Give the position of every leukocyte visible.
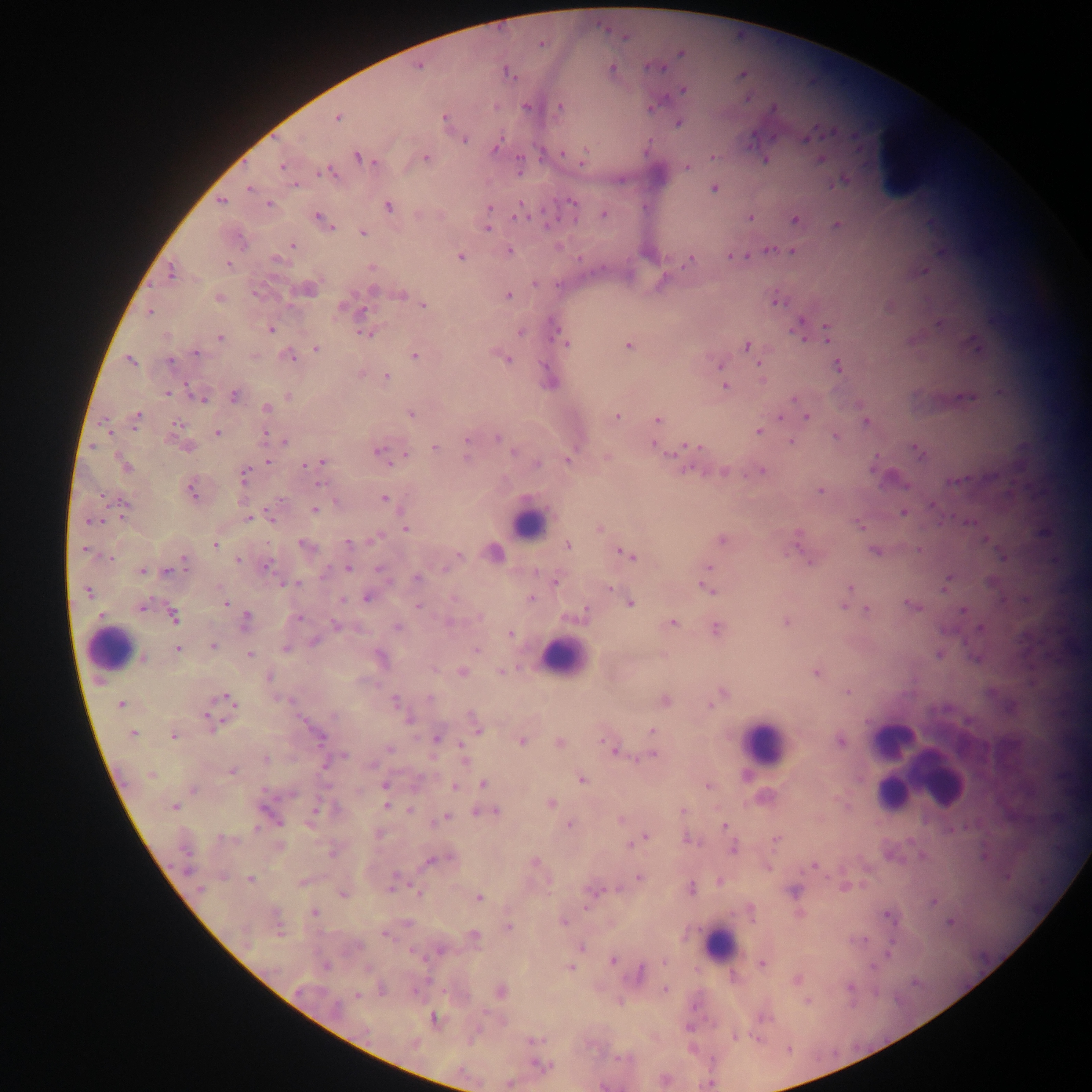

Approximate centers as (x, y) in pixels.
Leukocytes: (534, 523), (121, 652), (560, 660), (888, 740), (768, 750), (937, 779), (894, 795), (718, 946).

Summary:
  - Malaria parasite locations: (623, 37), (540, 44), (649, 66), (613, 67), (661, 67), (507, 72), (742, 74), (513, 79), (683, 90), (746, 99), (526, 105), (561, 105), (495, 106), (655, 106), (771, 110), (444, 117), (337, 118), (678, 123), (836, 132), (807, 139), (466, 140), (751, 144), (496, 146), (586, 150), (563, 153), (358, 156), (519, 158), (713, 158), (821, 158), (427, 159), (766, 160), (374, 161), (583, 162), (282, 166), (687, 166), (330, 167), (323, 172), (317, 174), (842, 179), (296, 184), (834, 184), (714, 187), (248, 189), (222, 200), (571, 201), (521, 202), (268, 203), (388, 205), (489, 207), (546, 207), (604, 213), (317, 215), (514, 216), (750, 217), (795, 219), (573, 221), (836, 224), (548, 225), (332, 228), (488, 228), (362, 232), (292, 245), (768, 249), (510, 250), (793, 250), (729, 255), (460, 256), (747, 256), (690, 260), (227, 264), (925, 270), (172, 273), (536, 284), (154, 285), (557, 285), (401, 296), (509, 296), (775, 302), (342, 306), (423, 306), (149, 311), (363, 311), (938, 323), (824, 324), (271, 330), (359, 331), (365, 332), (521, 333), (221, 337), (805, 337), (827, 341), (567, 345), (975, 345), (629, 346), (746, 346), (317, 349), (194, 352), (414, 356), (291, 357), (130, 360), (170, 360), (508, 360), (544, 364), (720, 364), (759, 364), (837, 364), (386, 376), (761, 379), (186, 384), (726, 386), (167, 392), (234, 395), (794, 398), (964, 398), (203, 400), (267, 408), (411, 414), (139, 415), (618, 416), (781, 417), (807, 417), (658, 420), (866, 421), (176, 424), (134, 427), (757, 431), (215, 432), (110, 433), (266, 433), (836, 436), (497, 437), (467, 439), (284, 441), (791, 441), (653, 444), (93, 446), (187, 446), (689, 446), (915, 446), (432, 447), (378, 449), (678, 450), (514, 451), (406, 455), (876, 455), (608, 456), (467, 457), (321, 460), (386, 460), (569, 460), (268, 461), (121, 462), (537, 462), (390, 463), (305, 465), (126, 466), (699, 470), (761, 470), (245, 472), (746, 473), (243, 479), (960, 480), (320, 483), (906, 485), (192, 487), (821, 490), (102, 496), (385, 499), (123, 500), (279, 500), (336, 501), (932, 505), (316, 510), (905, 512), (271, 516), (248, 517), (97, 520), (88, 522), (970, 522), (859, 525), (406, 529), (797, 532), (722, 539), (985, 539), (793, 540), (372, 541), (300, 543), (347, 543), (215, 545), (84, 549), (874, 550), (919, 550), (618, 551), (622, 554), (459, 555), (111, 557), (633, 557), (1002, 557), (182, 559), (237, 559), (809, 561), (269, 563), (709, 567), (348, 568), (185, 569), (378, 569), (445, 569), (143, 570), (327, 571), (949, 576), (416, 578), (281, 583), (298, 584), (703, 585), (219, 586), (849, 587), (945, 587), (611, 590), (712, 592), (88, 594), (531, 596), (367, 597), (152, 598), (452, 598), (343, 600), (905, 603), (630, 604), (226, 605), (843, 606), (418, 607), (917, 607), (140, 609), (866, 609), (962, 610), (101, 613), (247, 615), (300, 618), (479, 618), (786, 621), (452, 623), (673, 623), (335, 625), (397, 627), (717, 628), (980, 628), (511, 634), (312, 643), (212, 646), (179, 648), (476, 650), (249, 652), (939, 654), (977, 655), (433, 669), (462, 672), (500, 672), (815, 673), (848, 691), (429, 698), (213, 700), (233, 702), (395, 702), (121, 703), (712, 705), (408, 718), (223, 720), (478, 730), (652, 730), (323, 735), (173, 736), (436, 739), (603, 740), (840, 740), (522, 742), (559, 742), (608, 744), (460, 745), (389, 748), (615, 751), (344, 754), (653, 755), (636, 758), (265, 759), (465, 762), (372, 763), (232, 771), (581, 780), (482, 783), (385, 785), (708, 785), (455, 786), (328, 787), (193, 788), (262, 790), (293, 795), (836, 799), (552, 803), (386, 805), (175, 807), (409, 810), (495, 810), (316, 811), (475, 811), (683, 811), (446, 815), (620, 820), (280, 822), (569, 824), (726, 825), (256, 829), (950, 829), (645, 836), (220, 838), (775, 838), (638, 841), (630, 842), (733, 848), (189, 853), (331, 854), (535, 862), (813, 864), (768, 868), (189, 869), (223, 877), (639, 877), (1006, 878), (250, 879), (827, 880), (865, 883), (690, 885), (619, 887), (844, 888), (199, 890), (391, 890), (550, 891), (343, 895), (479, 898), (933, 902), (585, 907), (316, 912), (798, 914), (889, 914), (949, 921), (564, 922), (509, 925), (279, 933), (383, 934), (865, 939), (583, 946), (889, 953), (612, 961), (664, 961), (761, 964), (367, 966), (326, 967), (571, 967), (873, 968), (641, 972), (797, 978), (913, 983), (849, 987), (664, 988), (412, 992), (875, 992), (357, 994), (809, 1002), (485, 1013), (735, 1037), (757, 1040), (530, 1041), (787, 1049), (712, 1060), (539, 1065), (602, 1087)
  - Preparation: thick blood smear
  - Capture: mobile-phone photograph through a microscope
  - Field of view: single
  - Country: Ghana
  - Image size: 1092×1092 pixels